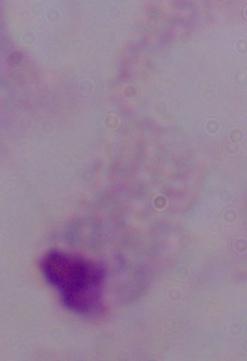

Summary:
  - Identification: trichomonad
  - Magnification: 1000x
  - Modality: photomicrograph